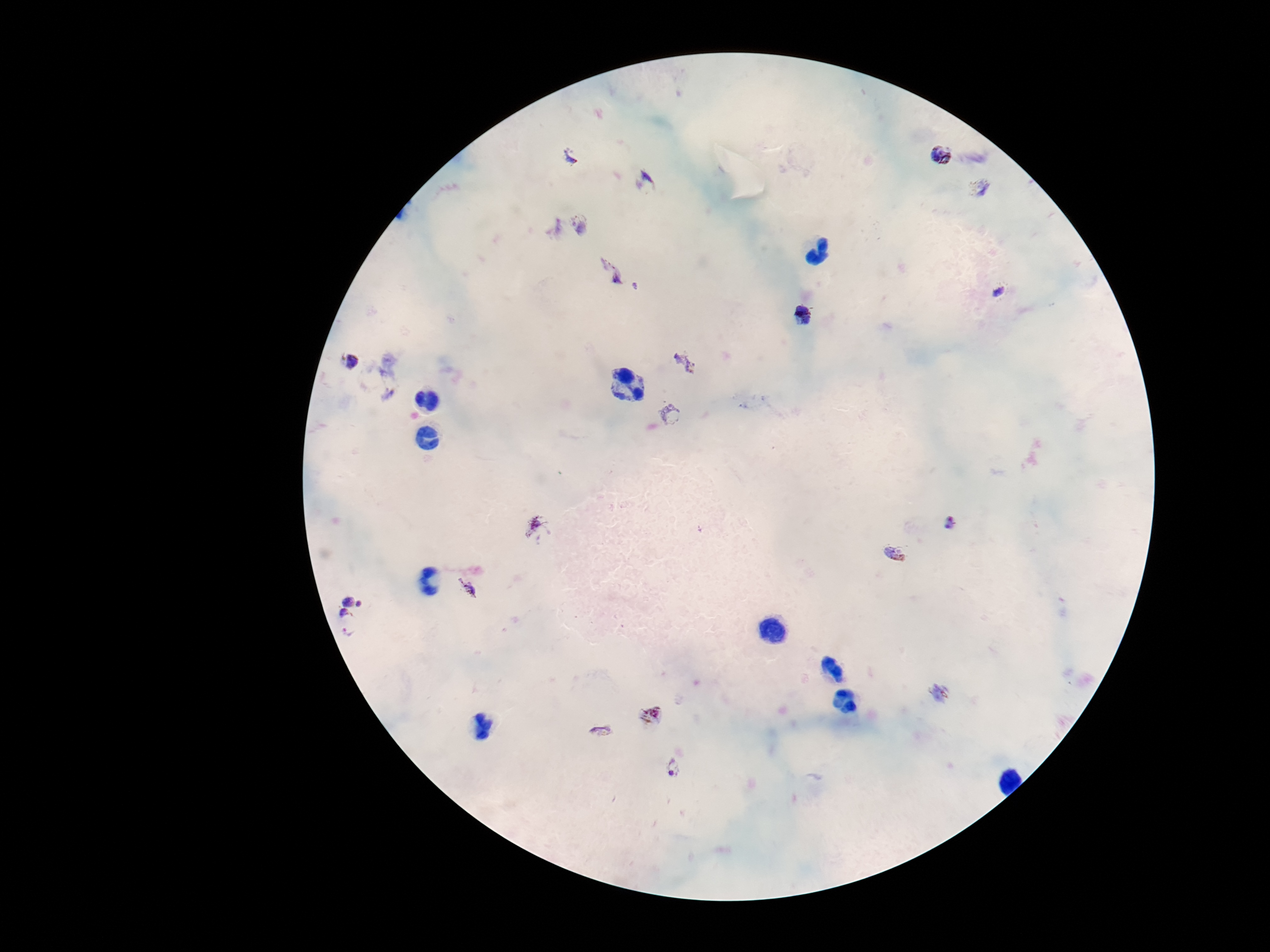
Approximate object centers, in pixels from the top-left corner. Plasmodium parasite locations: (x=943, y=154), (x=570, y=156), (x=645, y=183), (x=983, y=188), (x=582, y=224), (x=552, y=227), (x=610, y=270), (x=637, y=286), (x=997, y=291), (x=801, y=314), (x=352, y=361), (x=686, y=362), (x=669, y=414), (x=952, y=520), (x=538, y=528), (x=894, y=552), (x=466, y=589), (x=353, y=595), (x=344, y=614), (x=348, y=634), (x=940, y=694), (x=650, y=715), (x=599, y=730), (x=673, y=768). Image is 1270×952 pixels. 100x magnification. One field from this slide. Photographed through the microscope eyepiece with a smartphone camera. Patient malaria status: infected. Giemsa-stained preparation. Thick blood smear.